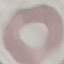
Result: negative for malaria parasites. Automatically extracted cell patch, resized to 64 × 64 pixels. Giemsa stain. Thin blood smear. Acquired by smartphone through the microscope eyepiece.